Name the parasite shown.
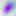

Toxoplasma gondii.

magnification: 400x
modality: photomicrograph